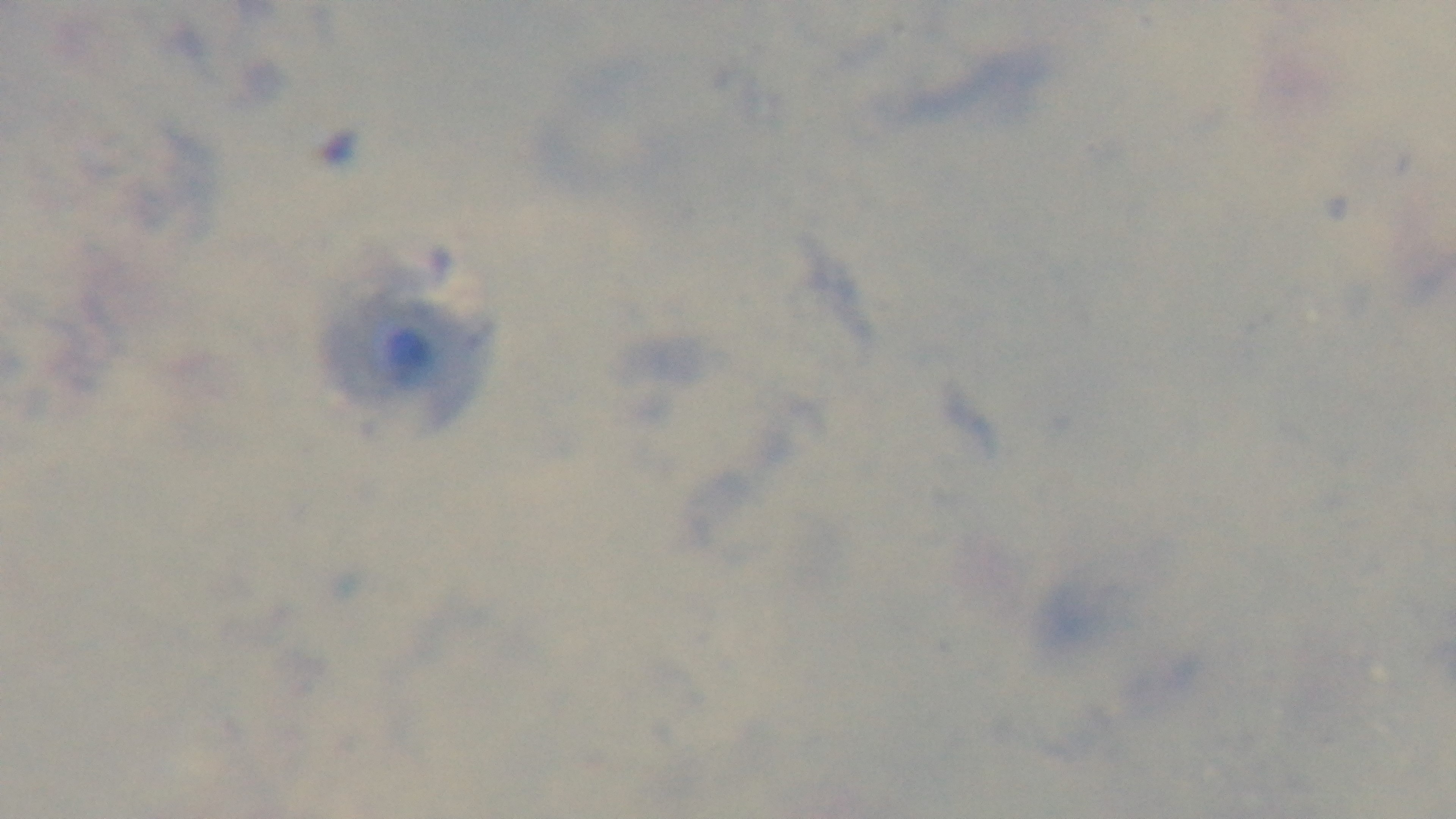
objective: 100x oil immersion
stain: Giemsa
capture: mounted 4K digital camera
preparation: thick smear
modality: light microscopy
field_of_view: single
malaria_status: uninfected